Locate every blood parasite and identify its species.
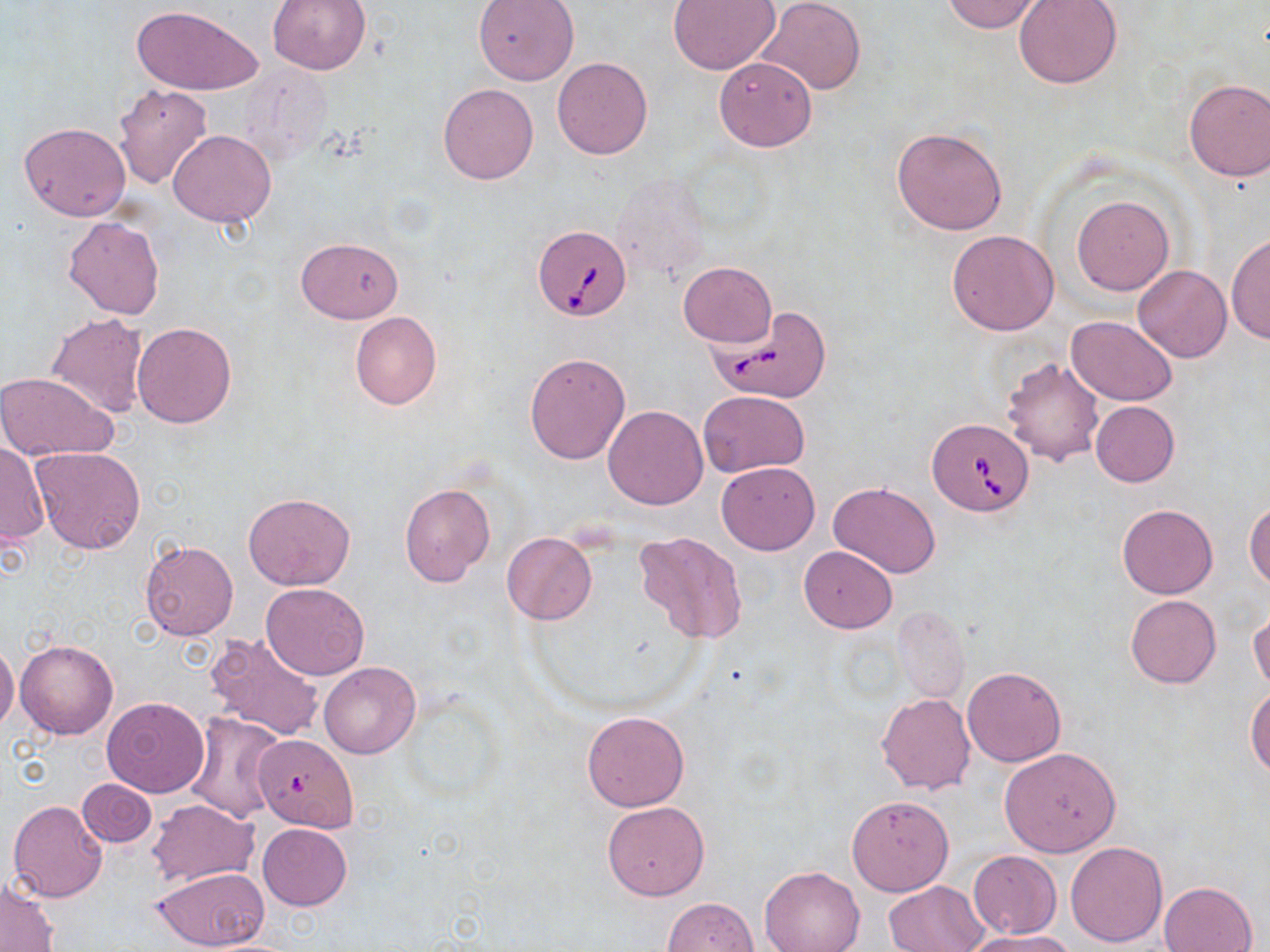

Approximate bounding boxes as (x1,y1)-(x2,y2) corner pairs in pixels.
Babesia divergens-infected red blood cells: (532,225)-(632,320), (708,306)-(833,403), (928,419)-(1034,515), (256,737)-(359,833).
No Plasmodium falciparum, Plasmodium ovale, Plasmodium malariae, Plasmodium vivax, or Trypanosoma brucei observed.

Uninfected red blood cell locations: (757,0)-(866,95), (940,0)-(1045,34), (1013,0)-(1123,88), (266,1)-(372,74), (473,1)-(579,85), (666,1)-(781,75), (133,4)-(262,96), (713,56)-(817,152), (551,57)-(652,159), (1183,78)-(1270,182), (438,83)-(538,184), (114,84)-(213,189), (18,121)-(130,222), (891,126)-(1009,235), (169,129)-(275,227), (610,171)-(711,285), (1072,195)-(1173,295), (63,216)-(165,320), (946,230)-(1058,335), (1226,233)-(1269,346), (296,238)-(403,323), (678,262)-(775,347), (1133,265)-(1233,362), (46,312)-(150,417), (350,312)-(442,410), (1066,316)-(1177,404), (132,321)-(236,428), (523,351)-(632,465), (1002,356)-(1105,466), (0,371)-(120,461), (698,391)-(809,477), (1089,401)-(1179,487), (604,406)-(708,509), (1,440)-(50,548), (30,447)-(146,553), (716,462)-(820,554), (398,482)-(497,588), (828,482)-(940,578), (243,492)-(355,589), (1244,500)-(1270,589), (1117,504)-(1218,599), (633,532)-(748,646), (502,533)-(596,623), (140,539)-(238,641), (799,545)-(898,632), (260,583)-(369,680), (1125,594)-(1221,688), (1249,606)-(1269,696), (894,607)-(969,705), (204,631)-(325,743), (15,639)-(118,740), (0,642)-(19,732), (318,661)-(421,759), (962,665)-(1067,767), (1247,685)-(1270,780), (877,693)-(975,793), (100,697)-(210,797), (582,710)-(689,811), (184,713)-(283,825), (998,747)-(1121,857), (76,778)-(156,849), (846,794)-(954,896), (8,799)-(108,902), (146,799)-(256,888), (602,801)-(709,900), (258,823)-(352,911), (1065,841)-(1167,947), (968,850)-(1061,938), (151,866)-(271,951), (760,866)-(865,952), (0,877)-(58,952), (884,880)-(986,952), (1160,881)-(1258,952), (662,897)-(758,952), (965,928)-(1079,951). Slide-level diagnosis: Babesia divergens. Optical microscopy. Thin blood film. Image is 1270×952 pixels. Single field of view. May-Grünwald-Giemsa-stained preparation. Captured at 1000x magnification.